Describe the morphology of the erythrocytes.
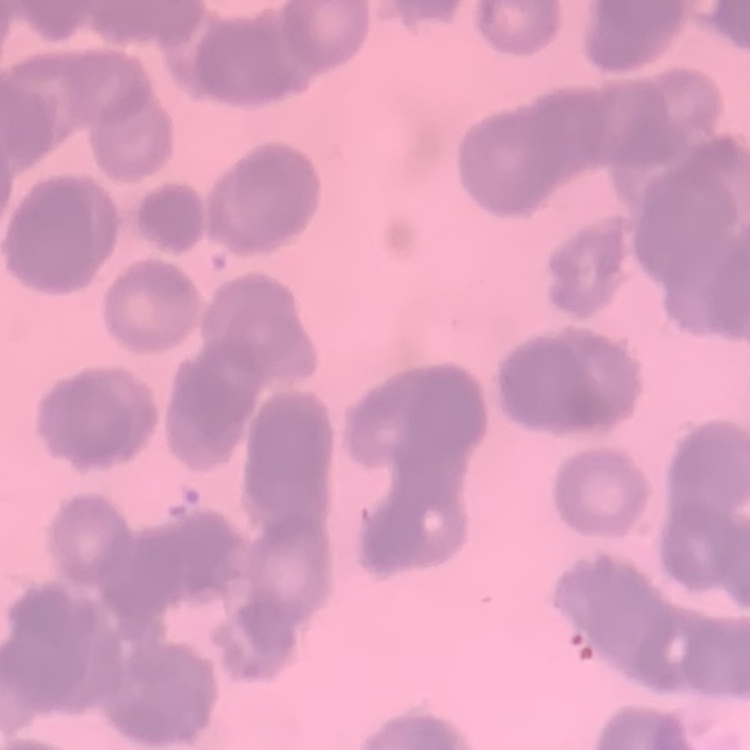

They show rouleaux formation.

One tile cut from a larger photomicrograph. Thin blood film. Field's or Giemsa stain.